Identify the parasite.
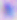

Toxoplasma gondii.

Captured at 400x magnification. Micrograph.